Classify this cell by malaria status.
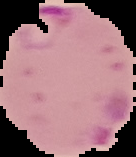

Parasitized.

From a thin blood smear. Image is 136×157 pixels. Cell region segmented out of the field of view; the surrounding area is masked to black.